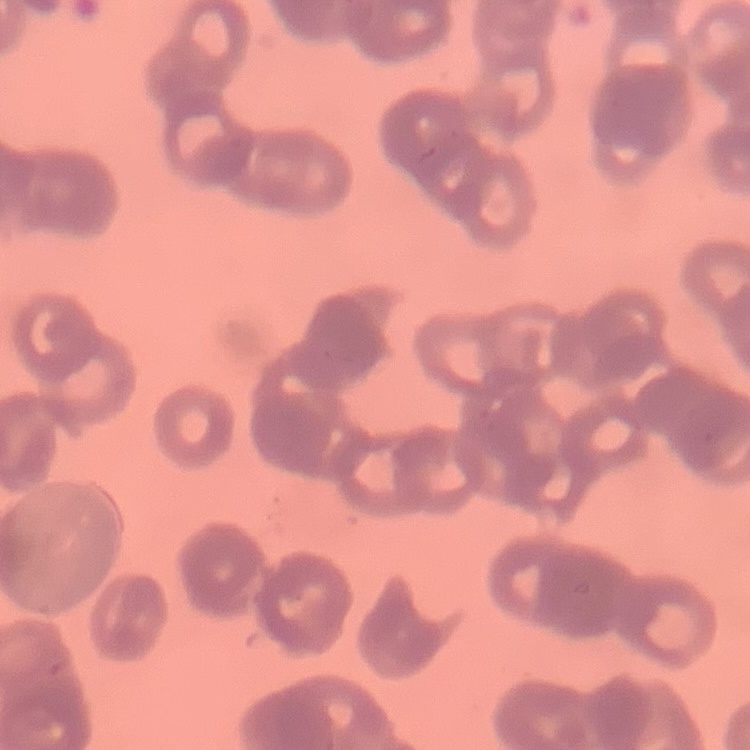
Summary:
  - Erythrocyte morphology: rouleaux formation
  - Stain: Field's or Giemsa
  - Preparation: thin peripheral smear
  - Image type: square crop of a larger photomicrograph